Locate every malaria parasite.
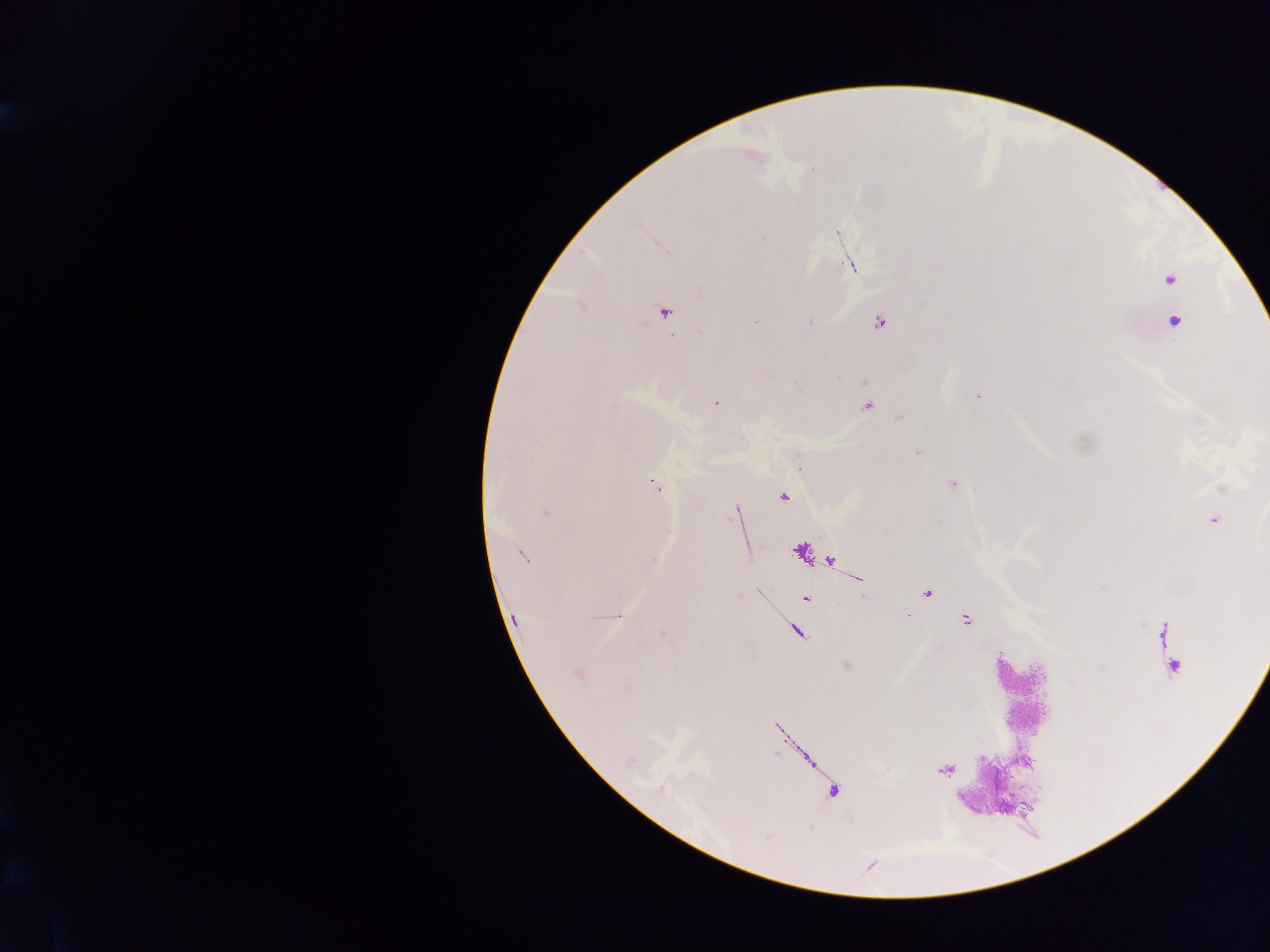
Approximate centers as x y in pixels.
Malaria parasites: 752 157; 836 232; 853 265; 1170 278; 581 304; 663 312; 755 321; 809 321; 1173 321; 879 322; 837 376; 864 382; 978 394; 715 402; 867 405; 900 417; 918 453; 952 483; 656 486; 782 495; 736 509; 545 512; 1213 518; 521 554; 828 560; 857 578; 759 592; 926 592; 805 598; 908 615; 965 619; 515 620; 796 631; 662 634; 1172 667; 578 673; 945 769.

Summary:
  - Preparation: thick blood smear
  - Image size: 1270×952 pixels
  - Country: Ghana
  - Capture: mobile-phone photograph through a microscope
  - Field of view: single